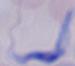

magnification: 1000x
identification: trypanosome
modality: photomicrograph